State the preparation type.
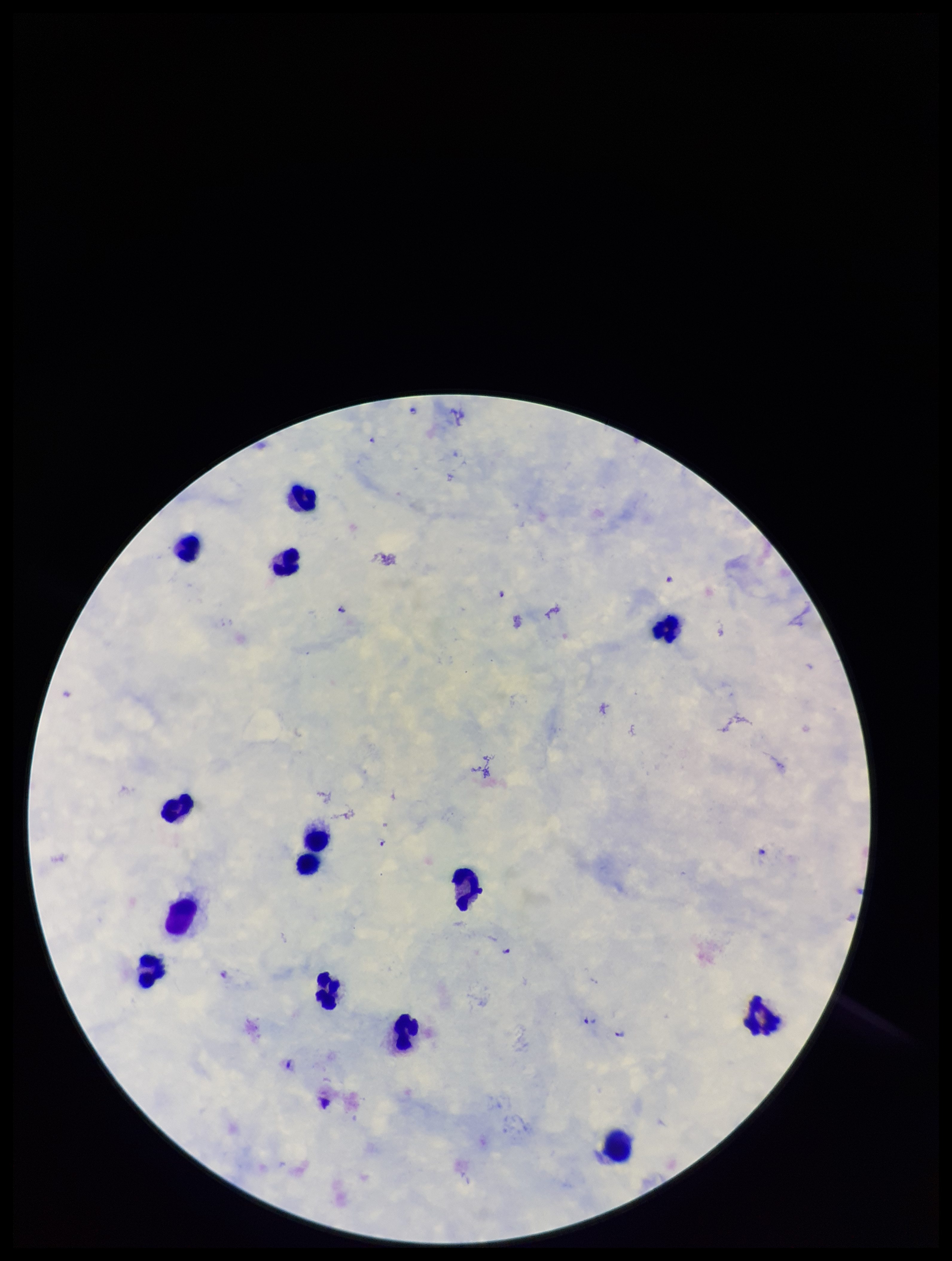
It is a thick blood smear.

Plasmodium parasites: identified. Parasite count: 8. Patient malaria status: infected. Image is 952×1261 pixels. Species reported for this patient: Plasmodium falciparum. Single field of view. Leukocyte count: 14. Stained with Giemsa. Smartphone photograph taken through the eyepiece of a microscope.